Locate and identify every blood parasite.
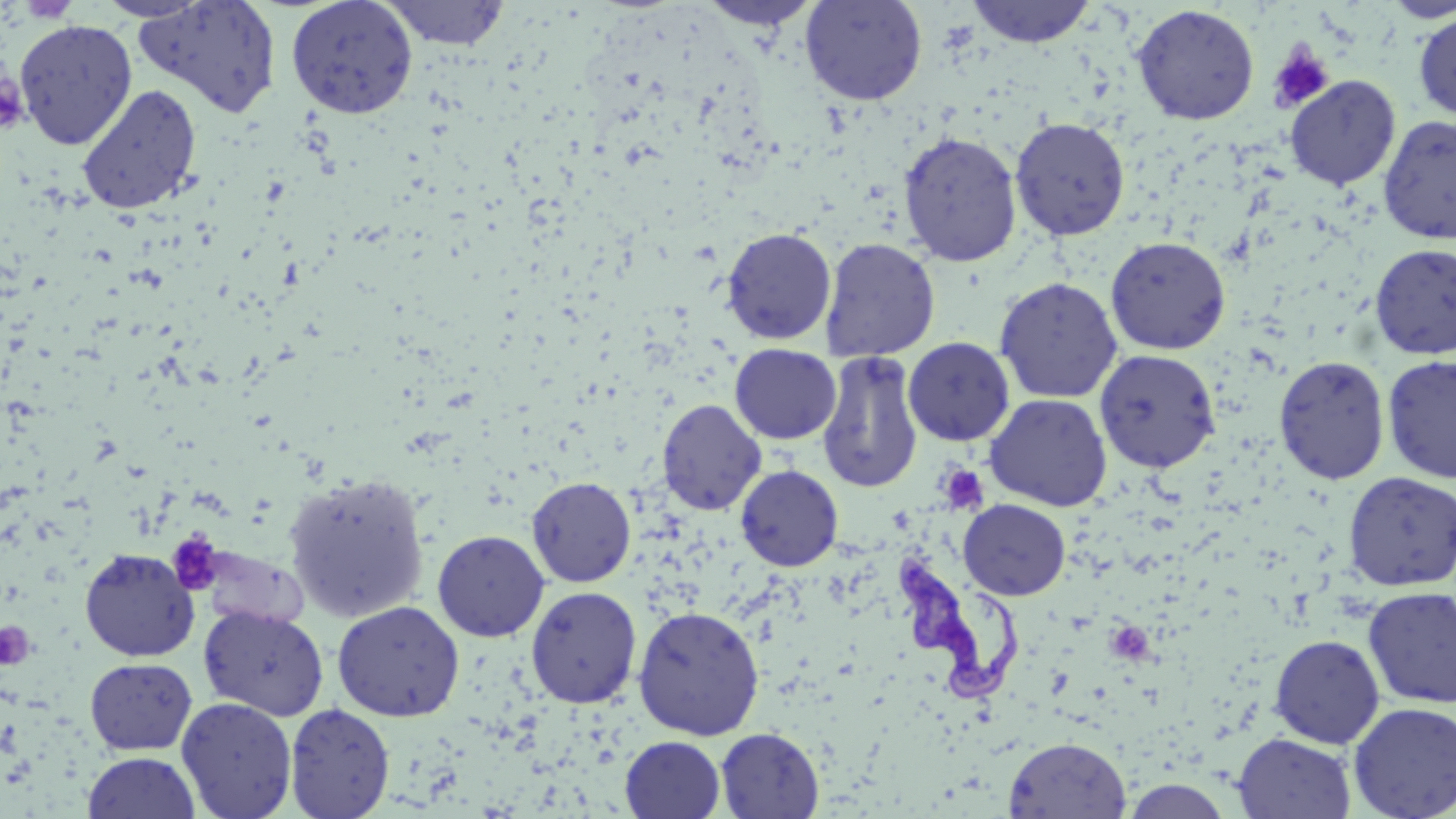
Approximate bounding boxes as (x1, y1, x2, y2) in pixels.
Trypanosoma brucei: (895, 553, 1030, 704).
No Plasmodium falciparum, Plasmodium ovale, Plasmodium malariae, Plasmodium vivax, or Babesia divergens observed.

Summary:
  - Uninfected red blood cell locations: (94, 0, 213, 22), (285, 0, 418, 118), (382, 0, 509, 50), (700, 0, 819, 32), (800, 0, 927, 106), (966, 0, 1097, 48), (1379, 0, 1456, 24), (132, 1, 282, 118), (1131, 4, 1260, 126), (1413, 11, 1456, 123), (14, 18, 138, 150), (1284, 75, 1401, 190), (77, 83, 202, 215), (1377, 114, 1456, 245), (1010, 116, 1130, 241), (896, 130, 1023, 268), (721, 226, 837, 345), (1105, 235, 1231, 355), (820, 238, 940, 362), (1369, 244, 1456, 359), (994, 277, 1123, 403), (903, 337, 1015, 446), (730, 344, 841, 445), (1094, 348, 1220, 472), (816, 350, 924, 494), (1273, 355, 1391, 484), (1382, 355, 1456, 483), (984, 393, 1113, 512), (658, 399, 766, 515), (735, 465, 843, 571), (1342, 471, 1456, 591), (282, 472, 431, 622), (526, 476, 636, 587), (958, 499, 1070, 600), (432, 529, 550, 642), (79, 548, 199, 662), (525, 585, 642, 708), (1363, 587, 1456, 708), (332, 600, 465, 721), (199, 605, 328, 720), (632, 605, 765, 740), (1268, 634, 1385, 749), (85, 658, 197, 755), (176, 697, 297, 819), (1348, 702, 1456, 819), (285, 703, 395, 819), (715, 727, 824, 818), (1233, 732, 1357, 819), (620, 736, 726, 819), (1004, 736, 1131, 818), (83, 752, 201, 819)
  - Platelet locations: (1267, 42, 1335, 114), (0, 70, 29, 134), (939, 466, 988, 514), (165, 531, 225, 597), (0, 621, 35, 670)
  - Slide-level diagnosis: Trypanosoma brucei
  - Preparation: thin blood film
  - Stain: May-Grünwald-Giemsa
  - Magnification: 1000x
  - Image size: 1456×819 pixels
  - Field of view: single
  - Modality: light microscopy